Evaluate for Plasmodium parasites.
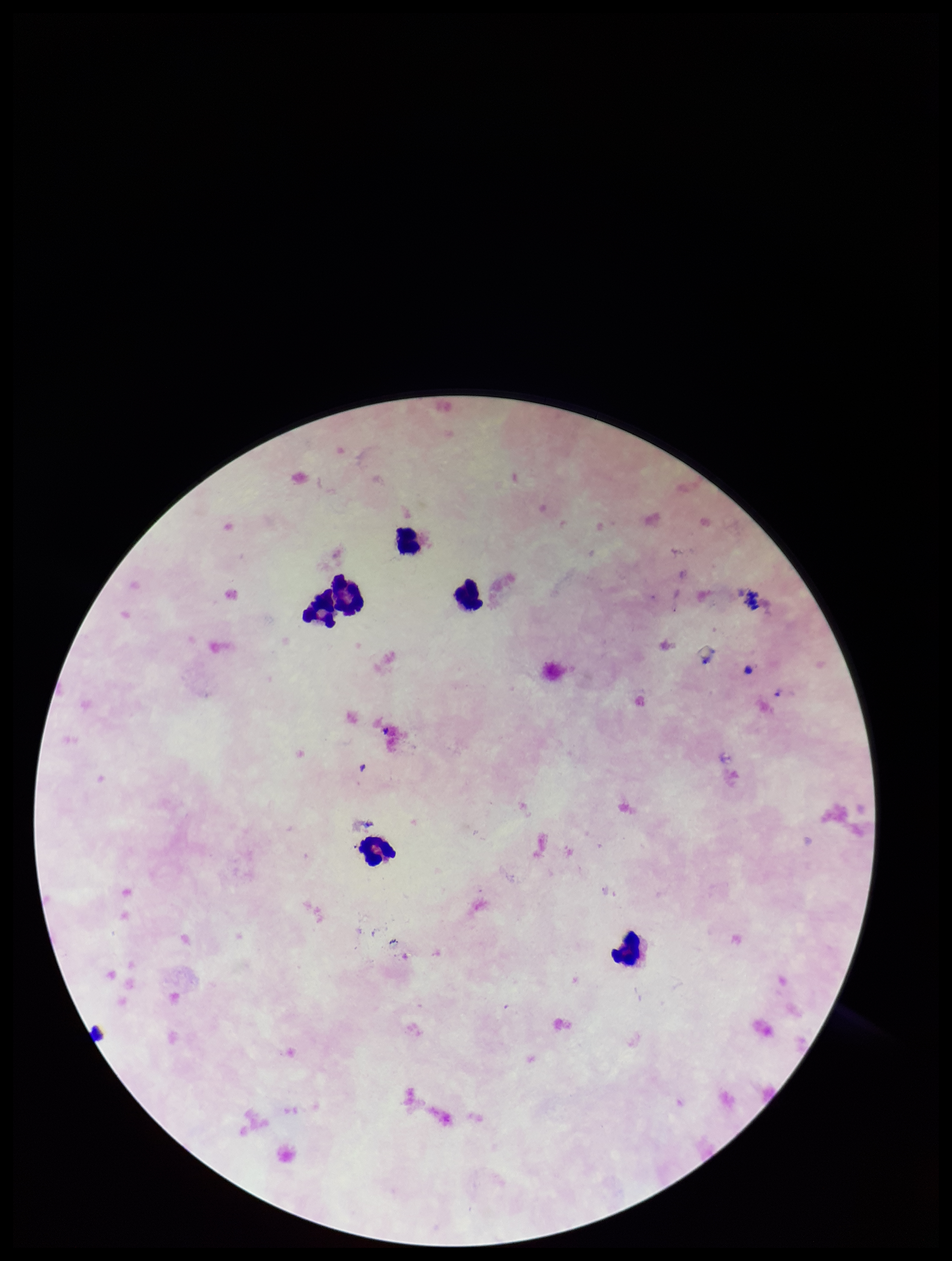
None detected.

Summary:
  - Parasite count: 0
  - Preparation: thick blood smear
  - Stain: Giemsa
  - Leukocyte count: 6
  - Patient malaria status: negative
  - Image size: 952×1261 pixels
  - Field of view: one from this slide
  - Capture: smartphone photograph through the microscope eyepiece